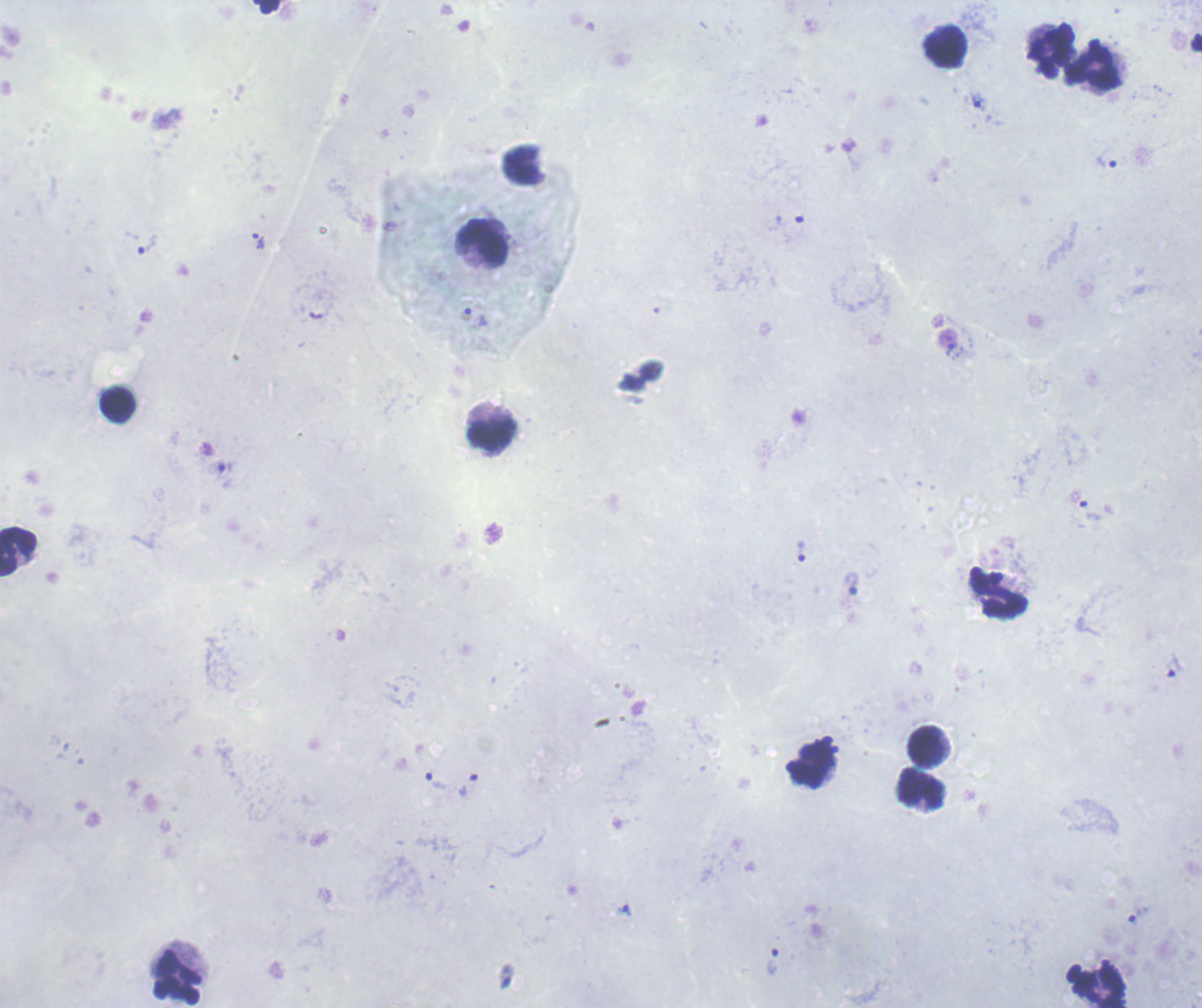
Approximate centers as [x, y] in pixels.
Summary:
  - Leukocyte locations: [266, 7], [945, 47], [1051, 51], [1095, 64], [484, 243], [118, 405], [491, 434], [18, 552], [998, 594], [927, 747], [809, 765], [921, 789], [177, 977], [1099, 987]
  - Trophozoite locations: [979, 102], [1107, 161], [789, 228], [258, 241], [148, 243], [1090, 511], [802, 551], [851, 582], [1172, 667], [437, 781], [469, 784], [625, 910], [773, 961]
  - Result: malaria parasites identified
  - Background quality: unsatisfactory
  - Stain: Romanowsky
  - Preparation: thick blood smear
  - Context: previously used in an actual diagnosis
  - Image size: 1202×1008 pixels
  - Magnification: 100x
  - Field of view: single